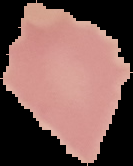
{
  "result": "no malaria parasites seen",
  "image_size": "133×166 pixels",
  "preparation": "thin blood film",
  "image_type": "cell region segmented out of the field of view; surrounding area masked to black"
}